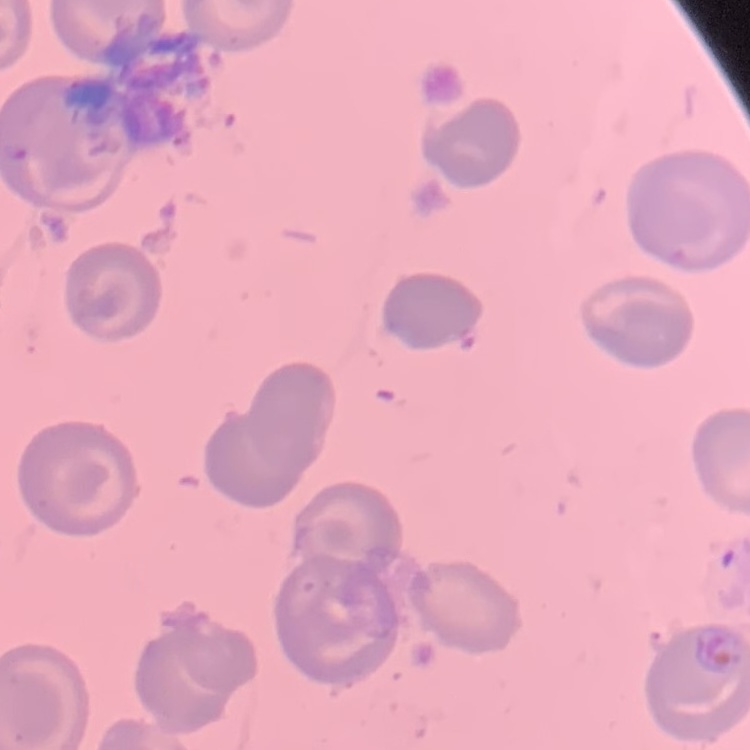

Summary:
  - Erythrocyte morphology: no rouleaux formation
  - Preparation: thin blood film
  - Image type: one tile cut from a larger photomicrograph
  - Stain: Field's or Giemsa